State the blood parasite species.
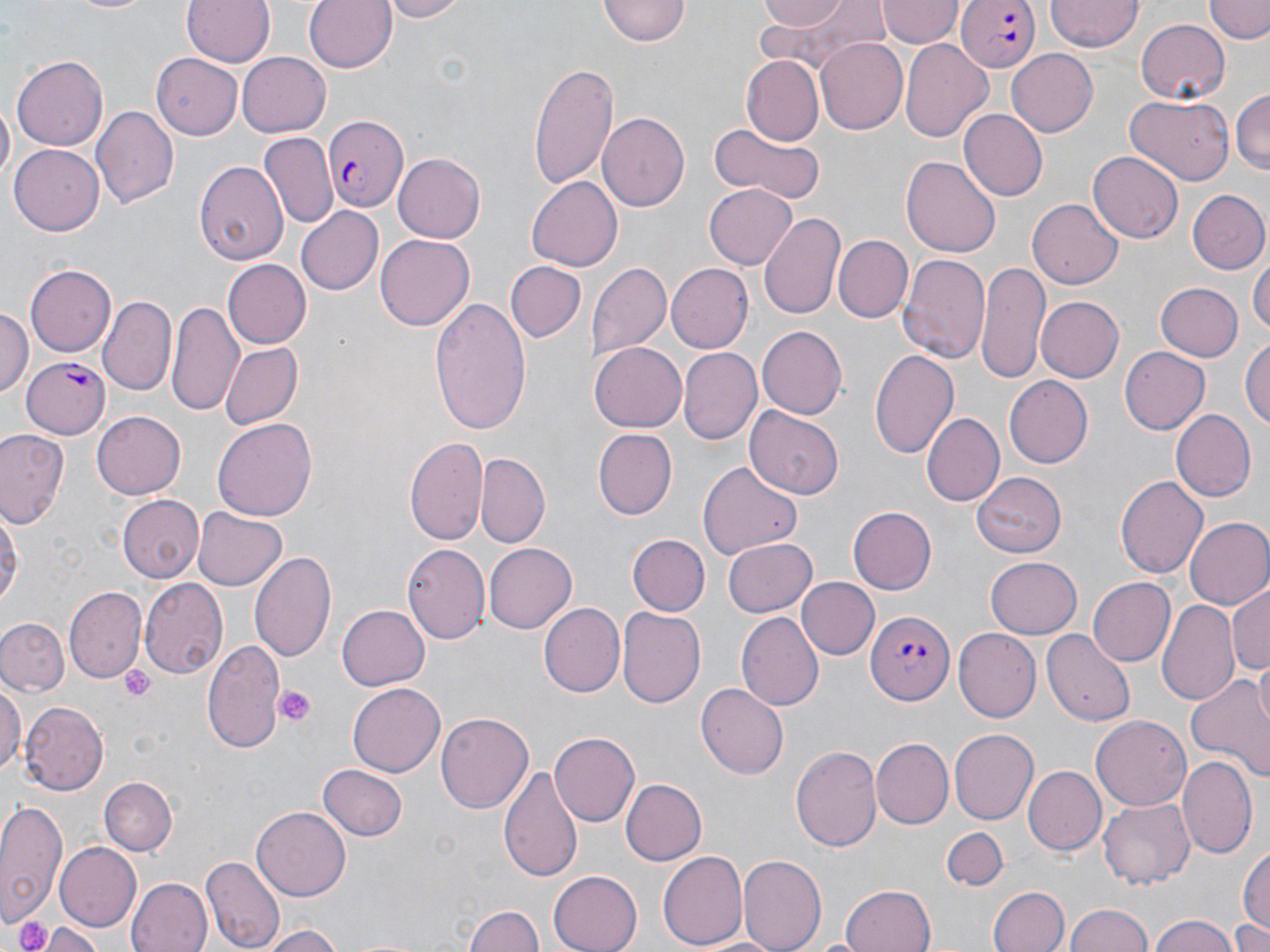

Plasmodium falciparum.

Approximate bounding boxes as (x1,y1)-(x2,y2) corner pairs in pixels. Uninfected red blood cell locations: (63,0)-(157,15), (182,0)-(275,67), (303,0)-(398,76), (380,0)-(468,23), (598,0)-(690,46), (751,0)-(860,30), (879,0)-(959,48), (1047,0)-(1142,53), (1204,0)-(1270,43), (1135,18)-(1228,106), (815,37)-(908,135), (900,38)-(993,145), (1007,48)-(1098,137), (152,53)-(241,140), (239,53)-(332,140), (12,55)-(109,150), (742,57)-(823,142), (529,64)-(616,194), (1231,87)-(1270,176), (1125,95)-(1234,184), (92,105)-(178,208), (961,110)-(1047,202), (598,111)-(690,211), (709,123)-(826,204), (259,134)-(337,230), (9,143)-(103,232), (1089,152)-(1183,243), (392,153)-(486,242), (900,156)-(1001,258), (194,159)-(289,266), (527,177)-(624,272), (705,182)-(799,269), (1187,190)-(1269,275), (1026,199)-(1123,289), (295,205)-(383,295), (759,210)-(846,323), (376,235)-(474,330), (835,235)-(912,323), (1251,253)-(1269,341), (899,254)-(990,365), (975,260)-(1050,384), (224,261)-(310,348), (505,261)-(585,342), (586,261)-(672,360), (665,263)-(752,353), (27,264)-(114,356), (1155,282)-(1243,361), (1034,294)-(1122,384), (98,296)-(176,396), (430,298)-(530,433), (167,301)-(242,414), (0,307)-(32,400), (756,325)-(847,420), (1242,335)-(1270,435), (589,342)-(686,433), (219,343)-(302,430), (678,346)-(761,443), (1119,346)-(1211,435), (868,347)-(959,459), (1006,375)-(1096,468), (747,408)-(843,499), (1170,409)-(1257,503), (90,411)-(184,500), (921,412)-(1003,506), (212,418)-(316,523), (590,428)-(676,520), (0,429)-(70,530), (405,435)-(486,545), (476,456)-(550,548), (698,462)-(802,558), (972,471)-(1070,558), (1115,474)-(1208,579), (117,495)-(203,584), (0,501)-(21,614), (848,506)-(937,595), (192,508)-(287,591), (1183,517)-(1270,609), (629,535)-(708,615), (723,538)-(817,617), (484,541)-(576,632), (402,543)-(490,646), (250,549)-(338,665), (986,556)-(1083,638), (139,577)-(227,679), (796,577)-(877,660), (1088,577)-(1175,665), (1230,584)-(1270,681), (64,588)-(144,682), (1158,598)-(1240,703), (537,603)-(623,697), (337,605)-(429,690), (616,608)-(703,710), (738,611)-(825,710), (0,618)-(70,696), (954,628)-(1041,721), (1043,632)-(1134,722), (201,635)-(285,752), (1185,666)-(1270,782), (0,680)-(24,778), (347,682)-(446,778), (696,684)-(789,779), (19,702)-(109,795), (436,712)-(534,812), (1092,713)-(1193,809), (550,730)-(639,826), (948,730)-(1037,824), (872,739)-(953,830), (791,744)-(883,854), (1179,754)-(1257,859), (498,762)-(585,885), (317,765)-(407,842), (1024,767)-(1105,854), (100,776)-(177,856), (621,777)-(706,865), (1098,798)-(1195,889), (0,799)-(67,927), (252,806)-(352,899), (942,828)-(1008,890), (1237,841)-(1270,946), (55,843)-(141,932), (659,850)-(748,950), (740,853)-(826,952), (203,854)-(284,952), (548,870)-(641,952), (126,877)-(211,952), (839,885)-(937,952), (989,886)-(1069,952), (1066,902)-(1152,952), (463,903)-(542,952), (1148,915)-(1244,952), (1233,919)-(1270,952), (41,923)-(106,952), (255,926)-(344,952). Plasmodium falciparum-infected red blood cell locations: (957,0)-(1039,73), (322,113)-(408,209), (22,358)-(111,438), (866,609)-(954,706). Platelet locations: (119,665)-(158,703), (273,685)-(317,729), (12,917)-(58,952). Single field of view. Image is 1270×952 pixels. May-Grünwald-Giemsa-stained preparation. Captured at 1000x magnification. Thin blood smear. Light microscopy.